Classify this cell by malaria status.
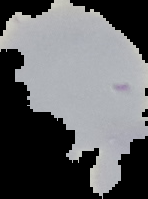
Uninfected.

preparation = thin blood film
image size = 148×199 pixels
image type = cell region segmented out of the field of view; surrounding area masked to black